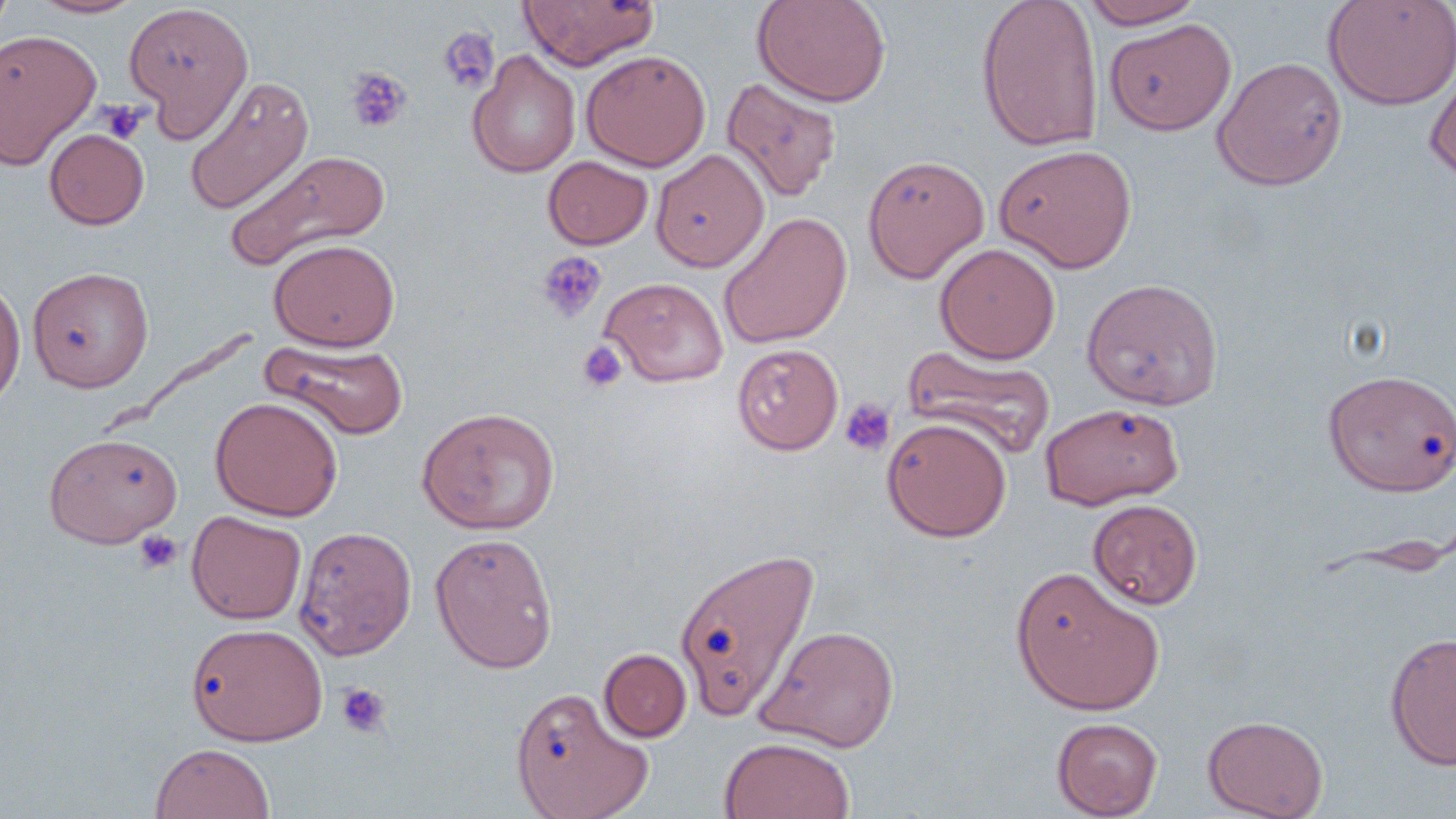
slide_level_diagnosis: negative for blood parasites
uninfected_red_blood_cell_locations: 'approximate bounding boxes as (x1, y1, x2, y2) in pixels: (0, 0, 15, 38), (28, 0, 145, 19), (751, 0, 891, 107), (975, 0, 1105, 153), (1323, 0, 1456, 111), (123, 1, 254, 138), (517, 1, 659, 70), (1079, 1, 1208, 29), (1104, 17, 1236, 135), (0, 29, 102, 169), (581, 49, 711, 171), (467, 50, 581, 178), (1212, 56, 1348, 191), (1425, 61, 1456, 181), (183, 76, 314, 214), (721, 76, 842, 202), (44, 128, 149, 229), (995, 144, 1137, 272), (225, 149, 389, 272), (651, 149, 769, 271), (863, 154, 989, 283), (543, 156, 653, 250), (719, 212, 853, 349), (269, 239, 399, 351), (935, 243, 1060, 363), (27, 266, 154, 392), (0, 274, 26, 412), (600, 277, 728, 386), (1082, 277, 1223, 410), (260, 338, 409, 441), (732, 343, 843, 455), (900, 346, 1059, 460), (1325, 368, 1455, 494), (210, 397, 342, 520), (1040, 402, 1184, 509), (417, 406, 561, 535), (882, 417, 1012, 542), (43, 432, 182, 547), (1087, 499, 1202, 609), (186, 511, 307, 624), (295, 525, 417, 660), (429, 532, 559, 674), (675, 544, 821, 722), (1010, 565, 1165, 717), (186, 623, 328, 745), (756, 624, 900, 753), (1384, 632, 1456, 771), (599, 648, 691, 741), (510, 686, 654, 819), (1203, 715, 1328, 819), (1051, 716, 1163, 818), (719, 736, 855, 819), (150, 743, 275, 819)'
modality: light microscopy
preparation: thin blood film
platelet_locations: 'approximate bounding boxes as (x1, y1, x2, y2) in pixels: (437, 27, 499, 95), (346, 68, 412, 134), (99, 100, 147, 144), (537, 252, 607, 324), (577, 340, 627, 392), (839, 399, 896, 456), (135, 530, 182, 575), (336, 683, 391, 737)'
magnification: 1000x
field_of_view: one of a larger specimen
image_size: 1456×819 pixels
stain: May-Grünwald-Giemsa